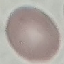
{
  "result": "no malaria parasites detected",
  "capture": "smartphone through the microscope eyepiece",
  "image_type": "automatically extracted cell patch, resized to 64 × 64 pixels",
  "preparation": "thin blood smear",
  "stain": "Giemsa"
}